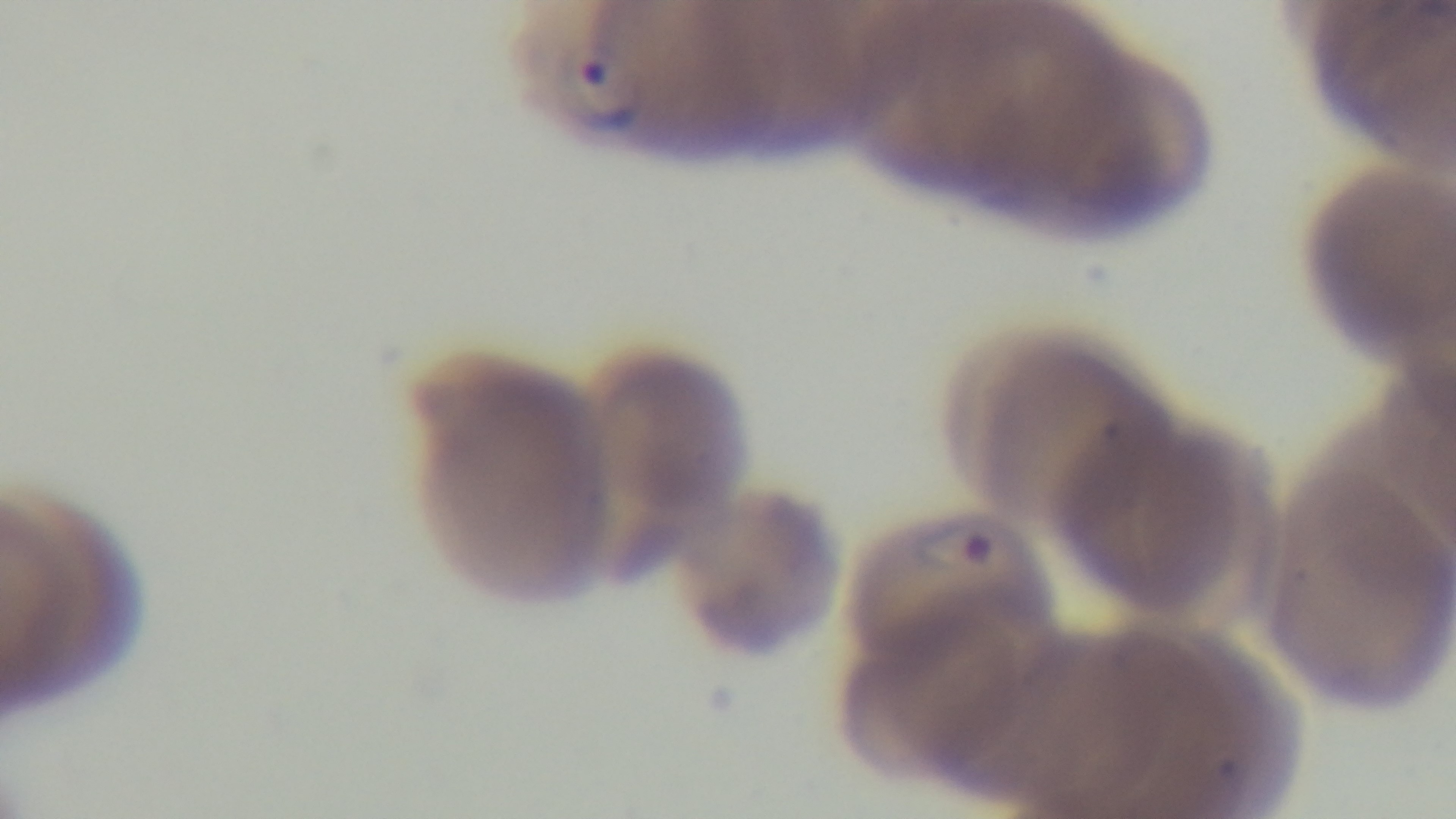 Captured with a mounted 4K digital camera. Malaria status: infected. Giemsa-stained. One field from the slide. Preparation: thin. 100x oil-immersion objective. Photomicrograph.